Outline each blood parasite and name the species.
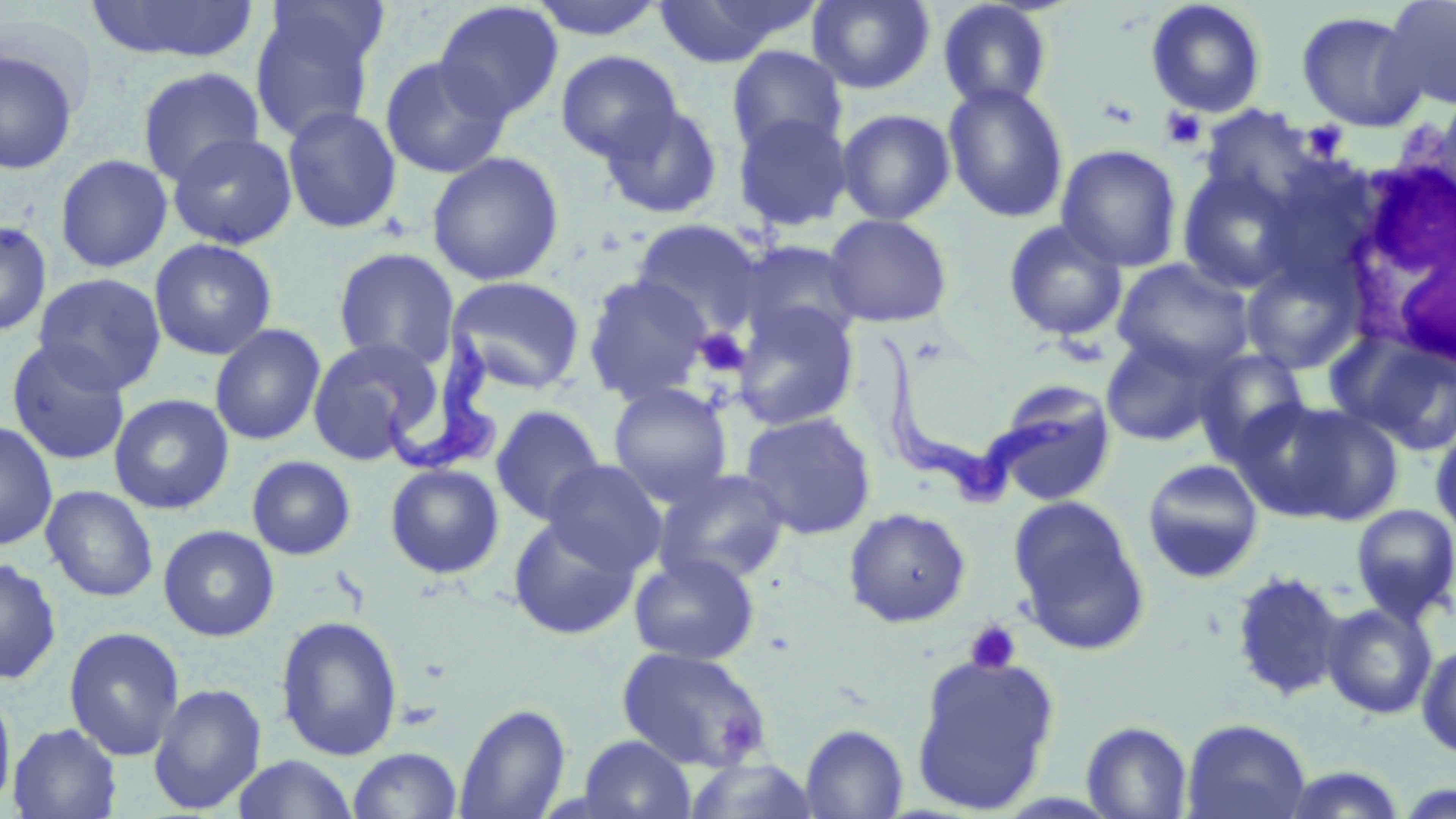
Approximate bounding boxes as named x1/y1/x2/y2 corners in pixels.
Trypanosoma brucei: (x1=383, y1=314, x2=504, y2=472), (x1=879, y1=332, x2=1078, y2=503).
No Plasmodium falciparum, Plasmodium ovale, Plasmodium malariae, Plasmodium vivax, or Babesia divergens observed.

Platelet locations: (x1=1161, y1=107, x2=1207, y2=149), (x1=1302, y1=121, x2=1348, y2=161), (x1=693, y1=328, x2=752, y2=378), (x1=964, y1=620, x2=1022, y2=675). White blood cell locations: (x1=1340, y1=151, x2=1456, y2=375). Uninfected red blood cell locations: (x1=86, y1=0, x2=261, y2=63), (x1=267, y1=0, x2=390, y2=76), (x1=527, y1=0, x2=669, y2=41), (x1=652, y1=0, x2=814, y2=67), (x1=807, y1=0, x2=936, y2=94), (x1=1380, y1=0, x2=1456, y2=110), (x1=937, y1=1, x2=1055, y2=112), (x1=1146, y1=1, x2=1266, y2=118), (x1=434, y1=2, x2=564, y2=122), (x1=249, y1=6, x2=380, y2=144), (x1=1296, y1=11, x2=1425, y2=132), (x1=726, y1=45, x2=848, y2=159), (x1=1, y1=48, x2=79, y2=174), (x1=556, y1=50, x2=682, y2=164), (x1=379, y1=55, x2=511, y2=179), (x1=137, y1=66, x2=266, y2=186), (x1=942, y1=82, x2=1070, y2=223), (x1=599, y1=101, x2=724, y2=219), (x1=282, y1=106, x2=402, y2=234), (x1=836, y1=108, x2=956, y2=225), (x1=732, y1=112, x2=853, y2=231), (x1=166, y1=131, x2=298, y2=250), (x1=1056, y1=144, x2=1182, y2=272), (x1=426, y1=151, x2=564, y2=286), (x1=54, y1=154, x2=173, y2=273), (x1=1176, y1=167, x2=1303, y2=294), (x1=823, y1=214, x2=953, y2=328), (x1=630, y1=219, x2=766, y2=338), (x1=0, y1=220, x2=52, y2=337), (x1=1003, y1=220, x2=1128, y2=341), (x1=149, y1=238, x2=277, y2=360), (x1=734, y1=240, x2=864, y2=349), (x1=333, y1=247, x2=460, y2=371), (x1=1240, y1=254, x2=1363, y2=374), (x1=1112, y1=258, x2=1253, y2=377), (x1=33, y1=272, x2=166, y2=395), (x1=582, y1=274, x2=714, y2=406), (x1=445, y1=275, x2=586, y2=394), (x1=730, y1=302, x2=860, y2=431), (x1=209, y1=324, x2=326, y2=446), (x1=1100, y1=332, x2=1224, y2=448), (x1=1331, y1=332, x2=1456, y2=453), (x1=306, y1=337, x2=440, y2=464), (x1=5, y1=340, x2=131, y2=466), (x1=1194, y1=348, x2=1311, y2=462), (x1=607, y1=383, x2=733, y2=505), (x1=989, y1=384, x2=1118, y2=507), (x1=108, y1=393, x2=234, y2=515), (x1=1247, y1=399, x2=1405, y2=525), (x1=490, y1=404, x2=607, y2=525), (x1=740, y1=411, x2=877, y2=540), (x1=0, y1=421, x2=58, y2=550), (x1=1430, y1=426, x2=1456, y2=537), (x1=246, y1=455, x2=356, y2=560), (x1=1142, y1=459, x2=1264, y2=583), (x1=543, y1=460, x2=667, y2=575), (x1=385, y1=463, x2=504, y2=579), (x1=655, y1=469, x2=791, y2=587), (x1=40, y1=485, x2=158, y2=602), (x1=1009, y1=496, x2=1149, y2=654), (x1=1351, y1=503, x2=1456, y2=623), (x1=844, y1=507, x2=971, y2=627), (x1=508, y1=515, x2=641, y2=640), (x1=158, y1=524, x2=280, y2=641), (x1=629, y1=552, x2=760, y2=666), (x1=0, y1=556, x2=61, y2=685), (x1=1229, y1=570, x2=1346, y2=702), (x1=1321, y1=602, x2=1438, y2=720), (x1=275, y1=614, x2=404, y2=760), (x1=63, y1=626, x2=185, y2=761), (x1=1417, y1=642, x2=1456, y2=759), (x1=617, y1=646, x2=772, y2=773), (x1=910, y1=653, x2=1060, y2=813), (x1=148, y1=683, x2=267, y2=814), (x1=0, y1=688, x2=16, y2=814), (x1=454, y1=703, x2=571, y2=819), (x1=1181, y1=718, x2=1312, y2=819), (x1=1082, y1=720, x2=1193, y2=818), (x1=8, y1=722, x2=122, y2=818), (x1=800, y1=723, x2=909, y2=819), (x1=577, y1=735, x2=696, y2=819), (x1=347, y1=747, x2=463, y2=819), (x1=231, y1=754, x2=359, y2=819), (x1=682, y1=758, x2=822, y2=817), (x1=1275, y1=766, x2=1409, y2=818), (x1=1393, y1=780, x2=1456, y2=817). Slide-level diagnosis: Trypanosoma brucei. Light microscopy. 1000x magnification. Image is 1456×819 pixels. May-Grünwald-Giemsa-stained preparation. One field of a larger specimen. Thin blood film.